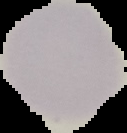 Cell region segmented out of the field of view; the surrounding area is masked to black. Malaria status: uninfected. Image is 127×133 pixels. From a thin blood smear.